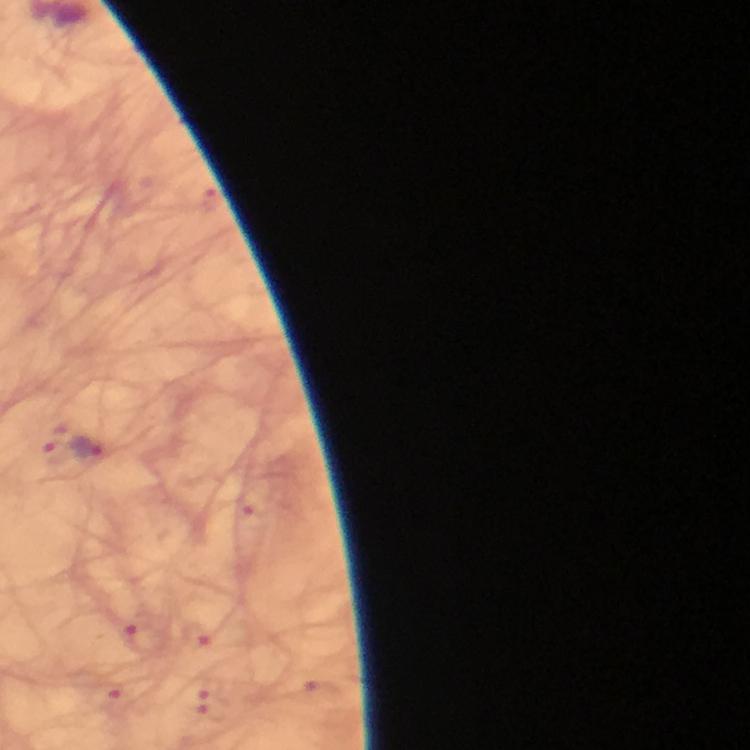
Approximate object centers, in pixels from the top-left corner.
Summary:
  - Malaria parasite locations: (x=86, y=451)
  - Magnification: 100x
  - Image size: 750×750 pixels
  - Preparation: thick blood film
  - Context: from a malaria diagnostic workup
  - Cropped from: a single field of view
  - Immersion oil: applied
  - Capture: smartphone photograph through a microscope
  - Stain: Giemsa